Locate every uninfected red blood cell.
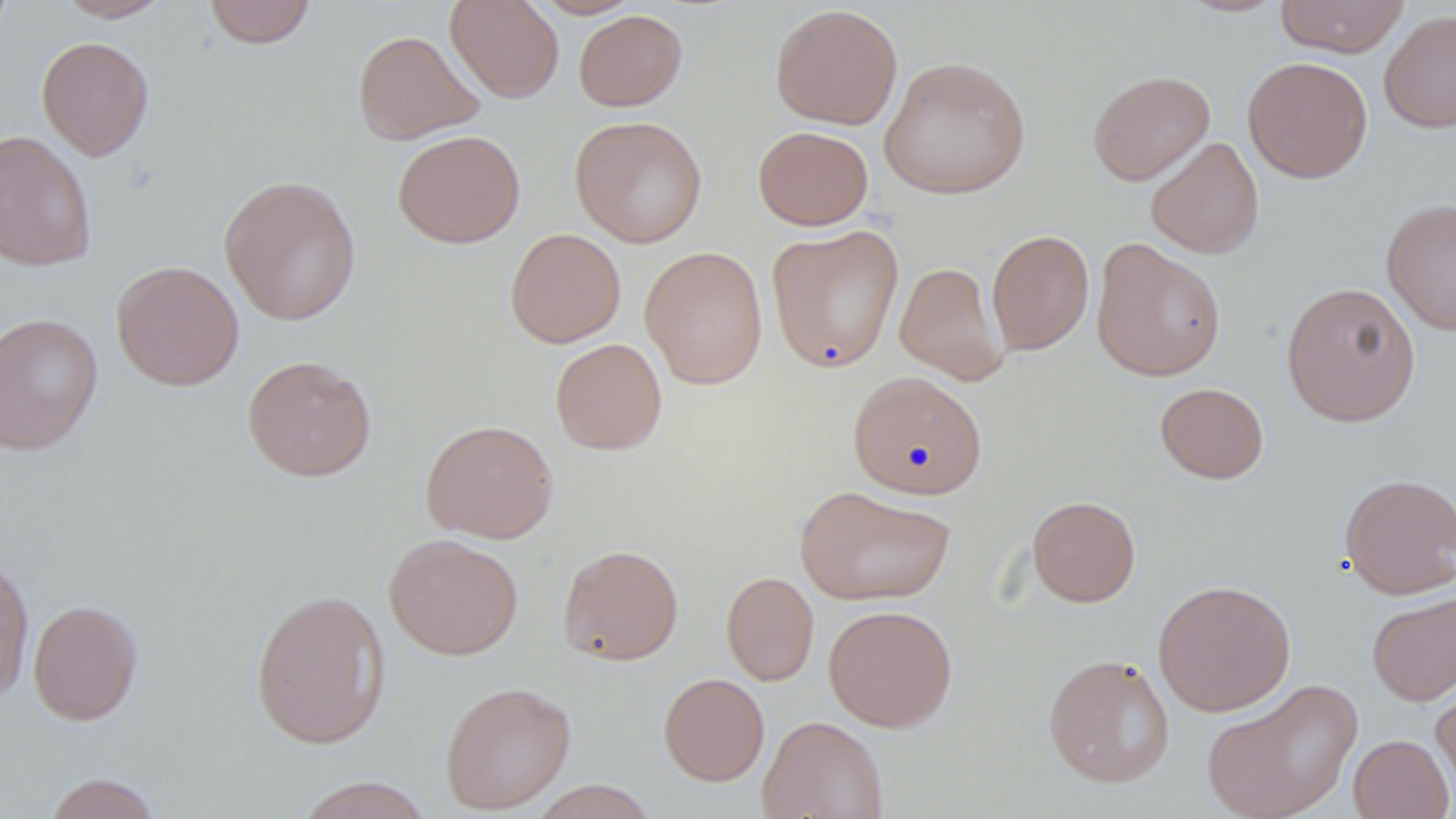
Approximate bounding boxes as [x1, y1, x2, y2] in pixels.
Uninfected red blood cells: [0, 0, 16, 47], [56, 0, 174, 21], [445, 0, 564, 103], [529, 0, 645, 19], [1275, 0, 1409, 57], [202, 1, 317, 48], [769, 4, 903, 130], [574, 9, 687, 111], [1379, 9, 1456, 134], [352, 30, 484, 144], [37, 36, 154, 161], [879, 56, 1031, 200], [1242, 56, 1372, 183], [1087, 70, 1215, 186], [569, 115, 708, 247], [753, 126, 874, 230], [0, 129, 97, 271], [393, 129, 525, 248], [1145, 137, 1264, 259], [218, 174, 362, 327], [1381, 197, 1456, 336], [766, 225, 904, 373], [504, 228, 625, 348], [986, 229, 1094, 355], [1090, 239, 1227, 382], [640, 246, 768, 390], [111, 260, 244, 390], [894, 261, 1008, 385], [1281, 281, 1421, 427], [0, 312, 103, 455], [550, 338, 667, 455], [241, 355, 377, 481], [848, 371, 987, 499], [1154, 382, 1269, 483], [420, 419, 558, 543], [1338, 472, 1456, 599], [795, 485, 957, 607], [1027, 495, 1141, 607], [384, 533, 523, 660], [557, 543, 684, 666], [0, 554, 35, 703], [721, 571, 819, 686], [1152, 579, 1296, 717], [250, 587, 391, 749], [1367, 590, 1456, 706], [27, 599, 143, 725], [823, 604, 958, 731], [1042, 653, 1175, 788], [659, 672, 770, 786], [1201, 678, 1363, 819], [439, 680, 576, 815], [1431, 681, 1456, 803], [757, 714, 889, 819], [1347, 734, 1454, 819], [41, 772, 164, 819], [290, 776, 436, 819], [527, 781, 662, 818].

slide-level diagnosis = negative for blood parasites
preparation = thin blood film
magnification = 1000x
stain = May-Grünwald-Giemsa
modality = optical microscopy
field of view = single
image size = 1456×819 pixels